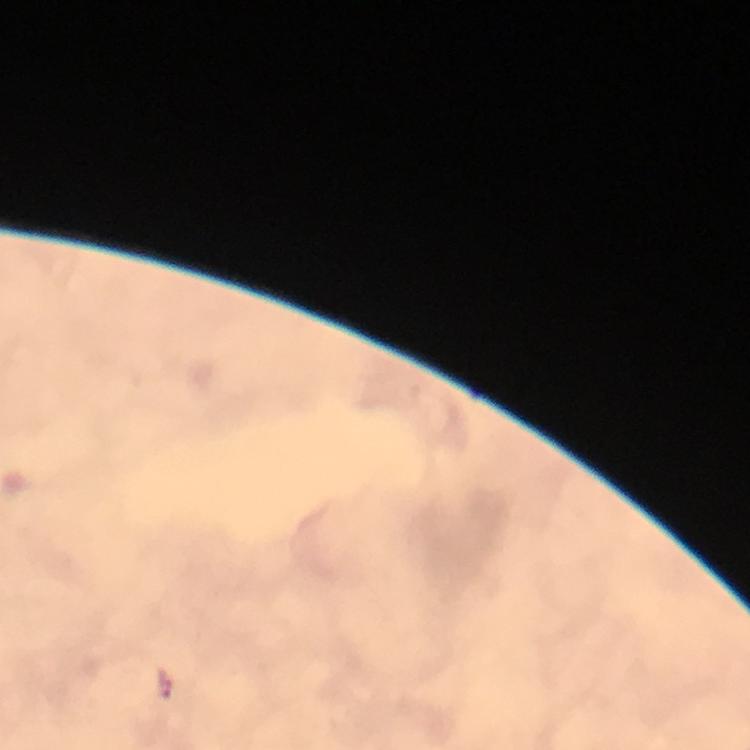

Approximate centers as (x, y) in pixels.
Summary:
  - Malaria parasite locations: (165, 686)
  - Magnification: 100x
  - Preparation: thick blood smear
  - Capture: smartphone mounted on the microscope
  - Stain: Giemsa
  - Context: from a diagnostic examination for malaria
  - Image size: 750×750 pixels
  - Immersion oil: used
  - Cropped from: a single field of view